Report the malaria status of this cell.
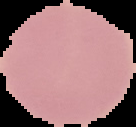
It is uninfected.

{
  "image_size": "136×127 pixels",
  "preparation": "thin blood smear",
  "image_type": "segmented cell region on a black background"
}